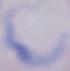 A trypanosome is seen. Captured at 1000x magnification. Micrograph.